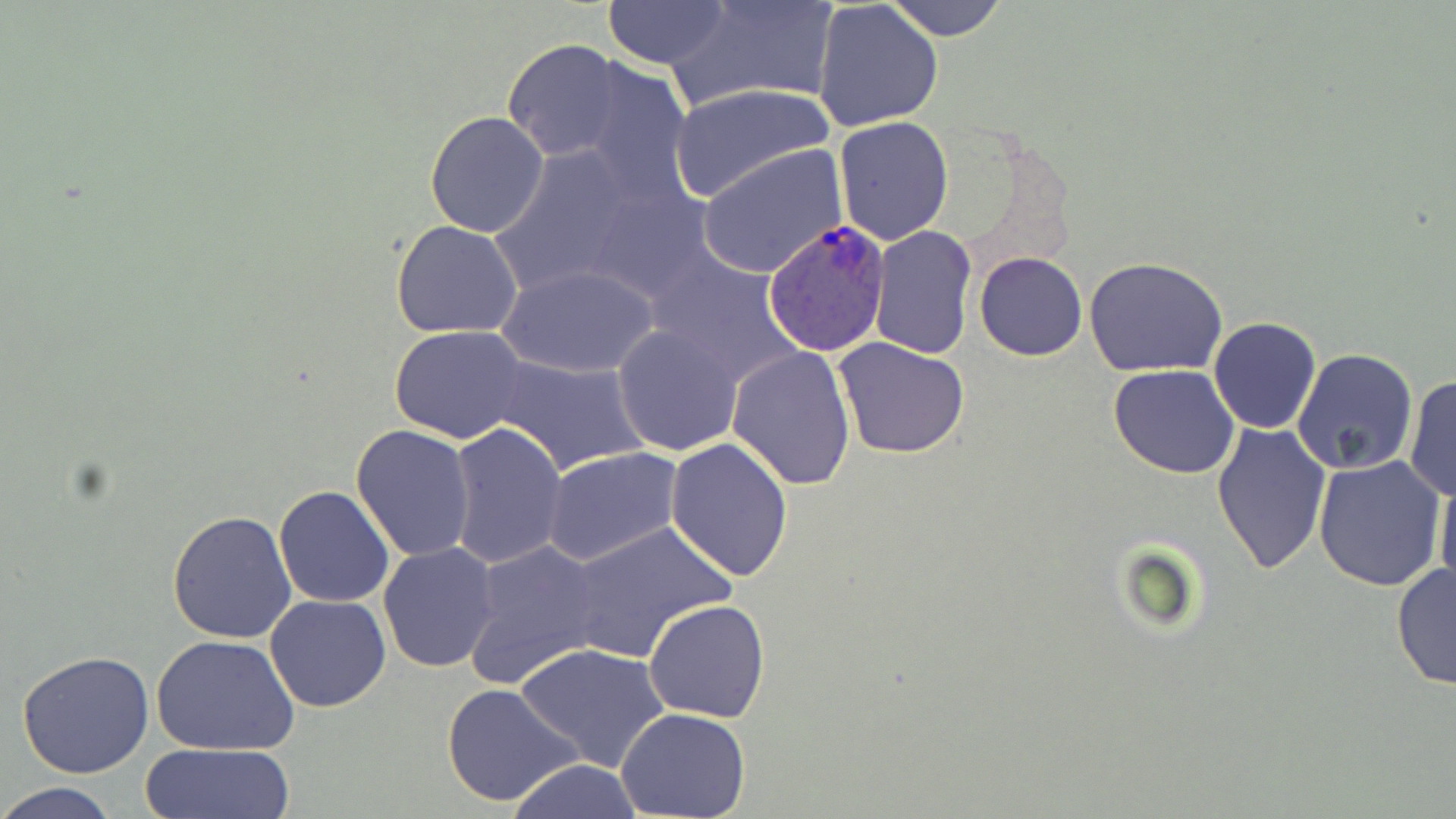

Plasmodium ovale-infected red blood cell locations = approximate bounding boxes as [x1, y1, x2, y2] in pixels: [764, 217, 891, 358]
slide-level diagnosis = Plasmodium ovale
stain = May-Grünwald-Giemsa
modality = light microscopy
magnification = 1000x
image size = 1456×819 pixels
field of view = single
uninfected red blood cell locations = approximate bounding boxes as [x1, y1, x2, y2] in pixels: [669, 0, 837, 109], [886, 0, 1007, 42], [603, 1, 731, 70], [813, 2, 944, 132], [502, 38, 626, 162], [580, 59, 698, 204], [671, 82, 835, 201], [425, 111, 549, 238], [834, 117, 956, 246], [489, 140, 651, 296], [698, 146, 847, 277], [391, 218, 525, 340], [868, 227, 976, 358], [645, 251, 793, 382], [975, 252, 1086, 360], [1083, 256, 1228, 376], [496, 264, 660, 380], [1208, 318, 1322, 435], [612, 326, 743, 456], [389, 327, 529, 443], [833, 338, 971, 459], [728, 347, 856, 491], [1292, 348, 1418, 475], [490, 355, 650, 475], [1108, 365, 1241, 478], [1403, 373, 1455, 501], [1212, 420, 1332, 576], [444, 421, 567, 570], [351, 423, 476, 561], [666, 438, 795, 580], [542, 447, 684, 567], [1312, 455, 1446, 592], [1434, 472, 1456, 590], [273, 486, 395, 608], [168, 511, 297, 644], [564, 521, 738, 659], [463, 540, 604, 687], [378, 542, 501, 672], [1391, 561, 1455, 691], [264, 594, 392, 713], [642, 599, 770, 722], [153, 636, 300, 755], [514, 642, 669, 773], [16, 649, 156, 780], [442, 683, 585, 808], [614, 708, 752, 818], [137, 742, 295, 819], [503, 759, 647, 818], [0, 781, 121, 819]
preparation = thin blood smear